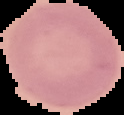

Summary:
  - Preparation: thin blood smear
  - Malaria status: uninfected
  - Image type: segmented cell region on a black background
  - Image size: 124×115 pixels